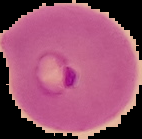
Segmented cell region on a black background. Image is 142×139 pixels. From a thin blood smear. Result: Plasmodium parasites detected.